Describe the morphology of the red blood cells.
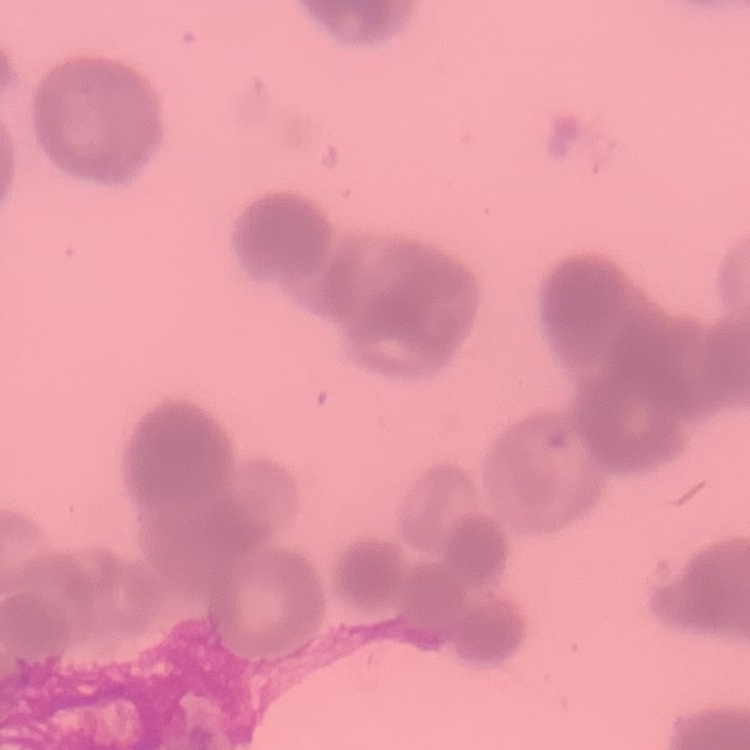
They show rouleaux formation.

Thin peripheral smear. Stained with either Field's or Giemsa. One tile cut from a larger photomicrograph.